Classify this cell by malaria status.
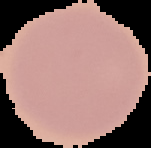

Uninfected.

Summary:
  - Image size: 151×148 pixels
  - Preparation: thin blood smear
  - Image type: segmented cell region on a black background